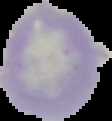
Summary:
  - Image size: 112×121 pixels
  - Image type: segmented cell region with the area outside set to black
  - Preparation: thin blood film
  - Result: no Plasmodium parasites detected